Locate every uninfected red blood cell.
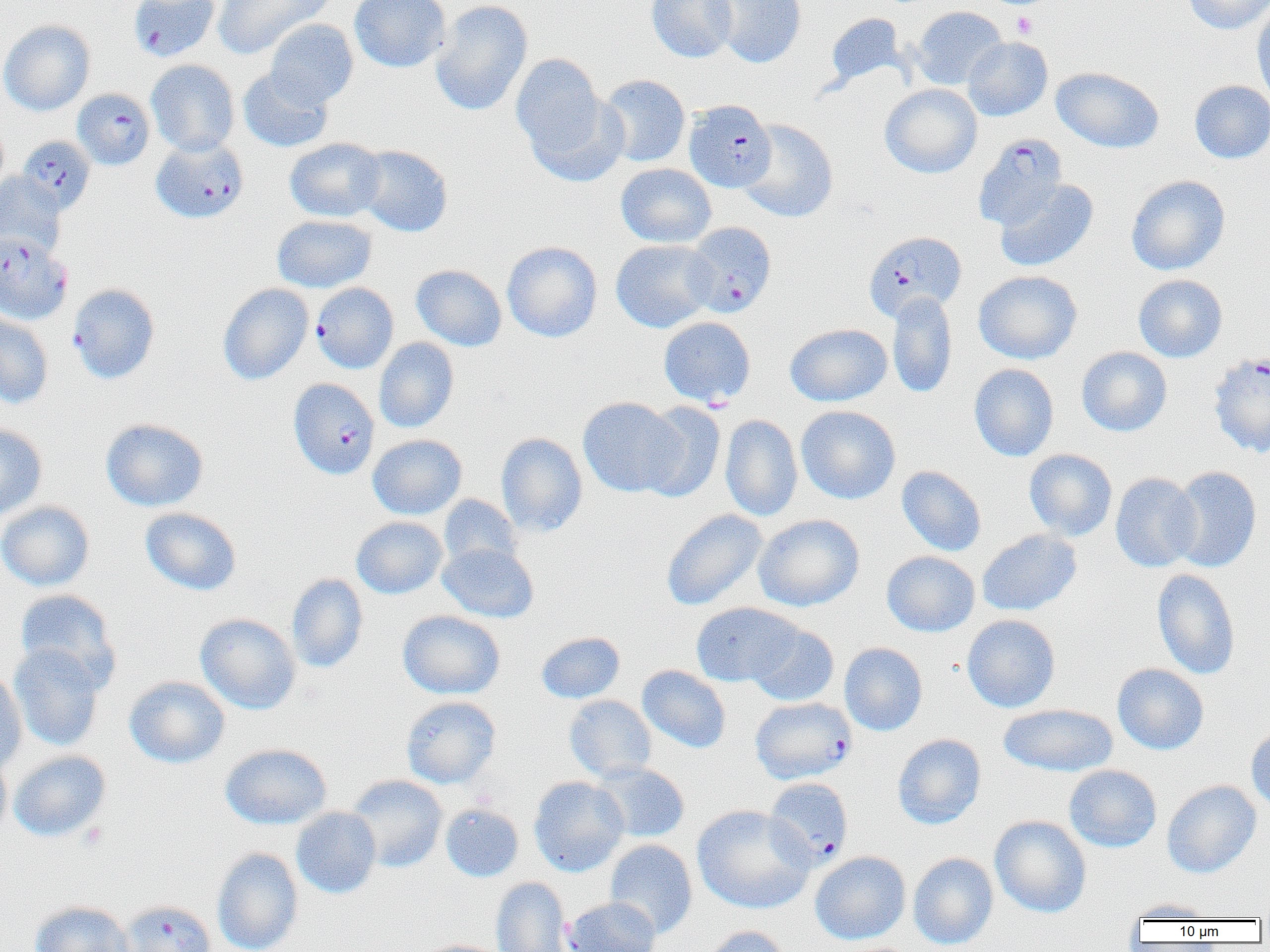

Approximate bounding boxes as (x1, y1, x2, y2) in pixels.
Uninfected red blood cells (subset): (212, 0, 335, 59), (349, 0, 451, 72), (430, 0, 533, 117), (647, 0, 737, 63), (709, 0, 807, 68), (1182, 0, 1270, 34), (1252, 3, 1270, 108), (911, 6, 1007, 89), (826, 13, 905, 88), (264, 19, 358, 108), (0, 20, 95, 116), (962, 37, 1053, 121), (511, 53, 607, 159), (146, 60, 240, 156), (238, 67, 334, 153), (1051, 67, 1164, 154), (598, 74, 690, 167), (1189, 80, 1270, 164), (880, 84, 981, 178), (525, 90, 628, 186), (738, 119, 838, 222), (284, 137, 386, 223), (353, 145, 453, 237), (616, 163, 716, 247), (0, 171, 65, 256), (1125, 175, 1230, 275), (994, 179, 1099, 272), (271, 214, 377, 293), (611, 239, 716, 333), (502, 240, 602, 342), (411, 264, 507, 351), (973, 270, 1082, 364), (1133, 274, 1227, 362), (217, 283, 314, 385), (887, 292, 957, 398), (0, 313, 53, 409), (659, 316, 755, 407), (784, 323, 892, 406), (374, 337, 459, 433), (1076, 346, 1172, 437), (969, 363, 1059, 461), (578, 396, 686, 497), (636, 402, 726, 503), (796, 405, 900, 504), (720, 414, 802, 521), (100, 418, 209, 512), (0, 423, 48, 520), (496, 432, 588, 537), (368, 434, 467, 519), (1024, 449, 1117, 540), (896, 465, 986, 556), (1168, 466, 1262, 572), (1109, 472, 1202, 573), (439, 494, 522, 571), (0, 500, 95, 591), (140, 507, 241, 596), (661, 509, 768, 611), (754, 514, 864, 611), (351, 516, 448, 599), (977, 529, 1081, 616), (437, 543, 539, 623), (881, 551, 980, 637), (1152, 568, 1240, 679), (286, 573, 368, 673), (15, 589, 121, 689), (691, 602, 801, 687), (397, 610, 505, 699), (195, 613, 301, 715), (962, 614, 1061, 712), (745, 621, 839, 706), (536, 631, 625, 704), (8, 643, 106, 752), (839, 643, 927, 735), (1112, 662, 1209, 755), (637, 665, 731, 753), (0, 668, 27, 776), (124, 675, 230, 768), (564, 695, 656, 782), (400, 696, 501, 789), (998, 703, 1118, 777), (1246, 725, 1270, 816), (892, 733, 986, 829), (220, 743, 332, 829), (9, 750, 111, 842), (0, 751, 11, 843), (592, 762, 690, 842), (1064, 765, 1162, 852), (346, 775, 448, 873), (529, 776, 629, 877), (1162, 780, 1262, 878), (441, 803, 524, 882), (692, 804, 815, 914), (291, 807, 381, 898), (990, 815, 1091, 917), (604, 838, 698, 939), (211, 847, 304, 952), (810, 851, 911, 944), (908, 851, 998, 950), (491, 877, 572, 951), (563, 897, 661, 952), (1125, 898, 1217, 921), (29, 900, 137, 952), (702, 926, 792, 952), (413, 939, 512, 952).

slide_level_diagnosis: Plasmodium falciparum
modality: optical microscopy
platelet_locations: 'approximate bounding boxes as (x1, y1, x2, y2) in pixels: (1011, 11, 1038, 39)'
plasmodium_falciparum_infected_red_blood_cell_locations_subset: 'approximate bounding boxes as (x1, y1, x2, y2) in pixels: (129, 0, 220, 62), (72, 88, 155, 170), (684, 99, 776, 192), (973, 134, 1067, 229), (17, 135, 95, 214), (151, 137, 248, 223), (683, 222, 776, 317), (863, 231, 966, 322), (0, 232, 72, 325), (68, 284, 159, 384), (289, 378, 379, 479), (750, 697, 857, 784), (765, 777, 854, 868), (120, 900, 215, 952)'
field_of_view: single
magnification: 1000x
image_size: 1270×952 pixels
preparation: thin blood film